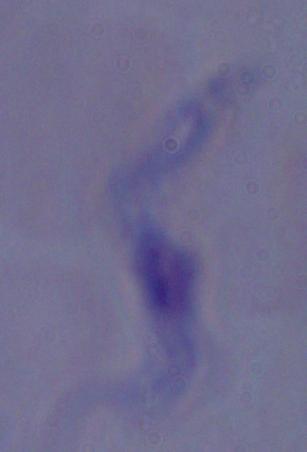
modality = micrograph
magnification = 1000x
identification = trypanosome